Outline each blood parasite and name the species.
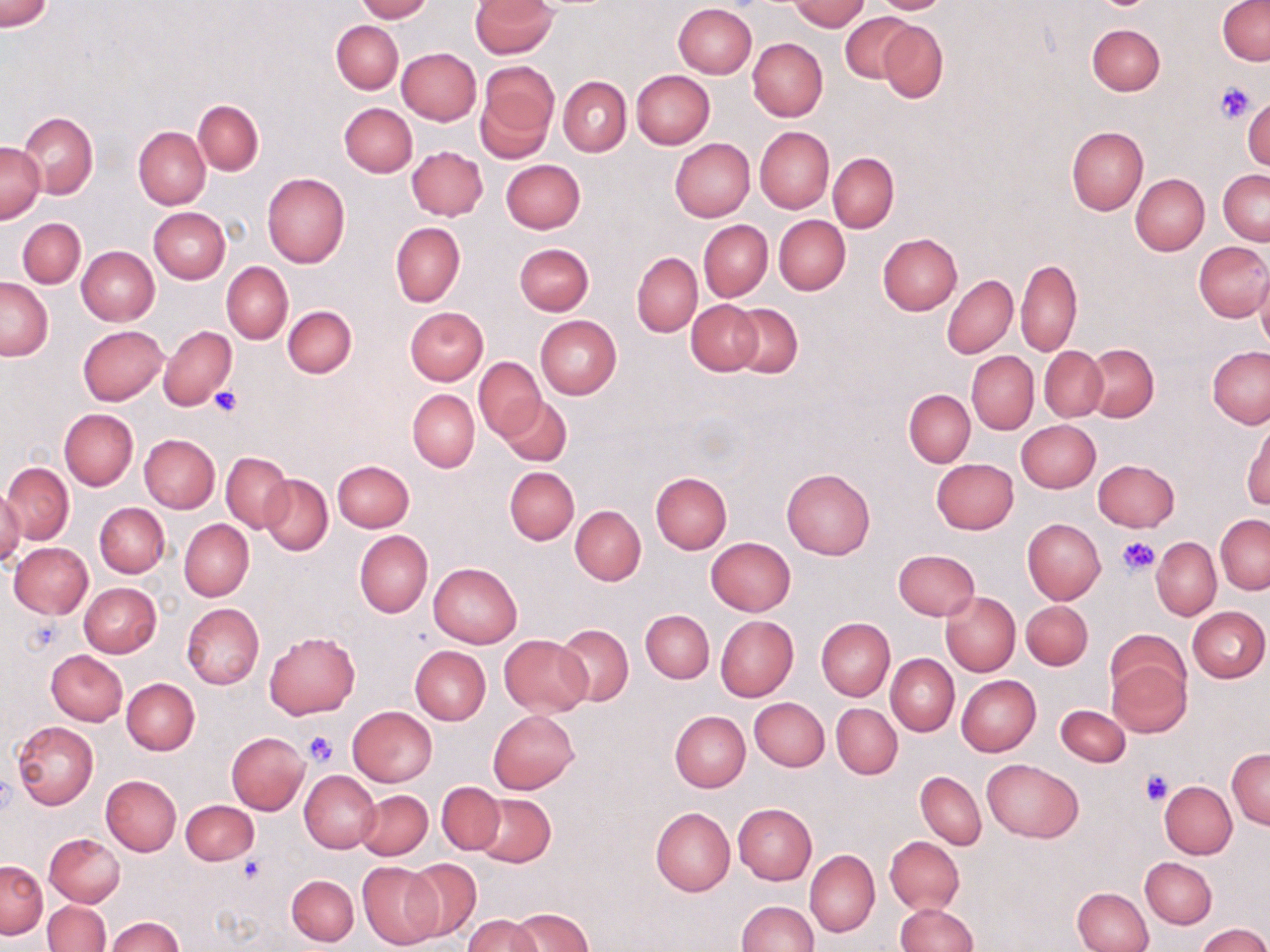

No blood parasites seen.

Summary:
  - Coordinate format: approximate bounding boxes as named x1/y1/x2/y2 corners in pixels
  - Uninfected red blood cell locations: (x1=0, y1=0, x2=54, y2=32), (x1=356, y1=0, x2=431, y2=21), (x1=471, y1=0, x2=556, y2=57), (x1=789, y1=0, x2=868, y2=31), (x1=868, y1=0, x2=953, y2=14), (x1=1218, y1=1, x2=1270, y2=66), (x1=673, y1=4, x2=757, y2=79), (x1=840, y1=12, x2=916, y2=85), (x1=878, y1=19, x2=948, y2=103), (x1=331, y1=20, x2=404, y2=93), (x1=1087, y1=24, x2=1164, y2=95), (x1=748, y1=38, x2=828, y2=122), (x1=397, y1=47, x2=480, y2=124), (x1=477, y1=63, x2=558, y2=158), (x1=631, y1=70, x2=715, y2=149), (x1=559, y1=76, x2=631, y2=156), (x1=1244, y1=97, x2=1269, y2=172), (x1=193, y1=100, x2=263, y2=175), (x1=340, y1=103, x2=417, y2=176), (x1=18, y1=113, x2=98, y2=197), (x1=1066, y1=126, x2=1148, y2=215), (x1=133, y1=127, x2=210, y2=209), (x1=754, y1=127, x2=834, y2=213), (x1=669, y1=138, x2=754, y2=221), (x1=1, y1=140, x2=45, y2=223), (x1=407, y1=146, x2=487, y2=220), (x1=828, y1=153, x2=898, y2=233), (x1=501, y1=159, x2=585, y2=234), (x1=1219, y1=170, x2=1270, y2=245), (x1=261, y1=172, x2=350, y2=268), (x1=1130, y1=174, x2=1209, y2=255), (x1=148, y1=207, x2=229, y2=283), (x1=774, y1=215, x2=850, y2=294), (x1=17, y1=218, x2=86, y2=287), (x1=699, y1=219, x2=772, y2=301), (x1=391, y1=223, x2=464, y2=306), (x1=877, y1=234, x2=962, y2=315), (x1=1194, y1=242, x2=1269, y2=321), (x1=513, y1=243, x2=593, y2=316), (x1=75, y1=246, x2=159, y2=326), (x1=632, y1=252, x2=702, y2=337), (x1=1016, y1=257, x2=1082, y2=356), (x1=222, y1=262, x2=293, y2=344), (x1=1256, y1=270, x2=1270, y2=355), (x1=943, y1=275, x2=1017, y2=358), (x1=1, y1=278, x2=52, y2=360), (x1=687, y1=300, x2=762, y2=375), (x1=726, y1=304, x2=802, y2=379), (x1=282, y1=305, x2=358, y2=378), (x1=405, y1=307, x2=489, y2=385), (x1=535, y1=315, x2=621, y2=399), (x1=78, y1=325, x2=166, y2=404), (x1=158, y1=325, x2=237, y2=411), (x1=1085, y1=344, x2=1159, y2=421), (x1=1208, y1=346, x2=1270, y2=429), (x1=1040, y1=347, x2=1107, y2=422), (x1=967, y1=351, x2=1039, y2=434), (x1=474, y1=357, x2=545, y2=441), (x1=408, y1=389, x2=480, y2=472), (x1=905, y1=389, x2=975, y2=467), (x1=499, y1=396, x2=572, y2=466), (x1=59, y1=409, x2=137, y2=489), (x1=1244, y1=419, x2=1270, y2=510), (x1=1016, y1=420, x2=1101, y2=493), (x1=140, y1=434, x2=220, y2=512), (x1=222, y1=453, x2=292, y2=532), (x1=930, y1=458, x2=1018, y2=534), (x1=1093, y1=459, x2=1179, y2=532), (x1=331, y1=460, x2=414, y2=532), (x1=3, y1=461, x2=74, y2=544), (x1=505, y1=467, x2=578, y2=544), (x1=782, y1=467, x2=875, y2=560), (x1=651, y1=472, x2=732, y2=553), (x1=260, y1=474, x2=333, y2=555), (x1=0, y1=488, x2=25, y2=566), (x1=95, y1=503, x2=169, y2=577), (x1=570, y1=505, x2=646, y2=585), (x1=1216, y1=514, x2=1270, y2=594), (x1=1022, y1=518, x2=1105, y2=604), (x1=180, y1=519, x2=253, y2=600), (x1=354, y1=530, x2=432, y2=618), (x1=706, y1=537, x2=795, y2=615), (x1=1152, y1=537, x2=1220, y2=619), (x1=10, y1=542, x2=94, y2=619), (x1=893, y1=549, x2=980, y2=620), (x1=429, y1=563, x2=522, y2=647), (x1=79, y1=583, x2=161, y2=658), (x1=941, y1=591, x2=1020, y2=676), (x1=1021, y1=600, x2=1093, y2=670), (x1=182, y1=603, x2=264, y2=689), (x1=1188, y1=606, x2=1268, y2=683), (x1=640, y1=609, x2=714, y2=683), (x1=715, y1=615, x2=798, y2=701), (x1=815, y1=618, x2=895, y2=701), (x1=555, y1=623, x2=633, y2=706), (x1=1106, y1=630, x2=1191, y2=701), (x1=264, y1=631, x2=360, y2=718), (x1=499, y1=634, x2=591, y2=716), (x1=410, y1=645, x2=490, y2=725), (x1=46, y1=650, x2=127, y2=725), (x1=886, y1=654, x2=959, y2=735), (x1=1107, y1=656, x2=1191, y2=738), (x1=956, y1=675, x2=1041, y2=756), (x1=123, y1=678, x2=199, y2=755), (x1=750, y1=697, x2=829, y2=771), (x1=831, y1=703, x2=902, y2=779), (x1=1055, y1=705, x2=1129, y2=766), (x1=348, y1=706, x2=438, y2=787), (x1=489, y1=710, x2=579, y2=793), (x1=670, y1=711, x2=750, y2=792), (x1=12, y1=721, x2=99, y2=809), (x1=226, y1=732, x2=308, y2=815), (x1=1227, y1=748, x2=1270, y2=828), (x1=983, y1=758, x2=1083, y2=841), (x1=299, y1=769, x2=381, y2=853), (x1=916, y1=771, x2=986, y2=849), (x1=100, y1=775, x2=180, y2=856), (x1=436, y1=781, x2=505, y2=854), (x1=1159, y1=781, x2=1237, y2=859), (x1=356, y1=789, x2=432, y2=860), (x1=473, y1=794, x2=555, y2=867), (x1=180, y1=801, x2=258, y2=865), (x1=733, y1=803, x2=817, y2=885), (x1=651, y1=807, x2=734, y2=895), (x1=44, y1=833, x2=123, y2=907), (x1=885, y1=836, x2=964, y2=913), (x1=805, y1=849, x2=879, y2=937), (x1=1141, y1=857, x2=1217, y2=929), (x1=403, y1=859, x2=482, y2=942), (x1=1, y1=860, x2=47, y2=938), (x1=357, y1=862, x2=443, y2=949), (x1=286, y1=874, x2=359, y2=946), (x1=1073, y1=887, x2=1152, y2=952), (x1=44, y1=900, x2=110, y2=951), (x1=735, y1=900, x2=817, y2=952), (x1=894, y1=903, x2=976, y2=952), (x1=509, y1=907, x2=594, y2=951), (x1=464, y1=914, x2=541, y2=952), (x1=106, y1=916, x2=184, y2=952), (x1=1197, y1=924, x2=1269, y2=952)
  - Platelet locations: (x1=1211, y1=80, x2=1258, y2=123), (x1=209, y1=385, x2=242, y2=417), (x1=1118, y1=537, x2=1160, y2=575), (x1=22, y1=619, x2=61, y2=657), (x1=302, y1=730, x2=339, y2=769), (x1=1140, y1=771, x2=1174, y2=805), (x1=238, y1=856, x2=266, y2=883)
  - Slide-level diagnosis: negative for blood parasites
  - Preparation: thin blood film
  - Image size: 1270×952 pixels
  - Magnification: 1000x
  - Modality: optical microscopy
  - Field of view: one of a larger specimen
  - Stain: May-Grünwald-Giemsa